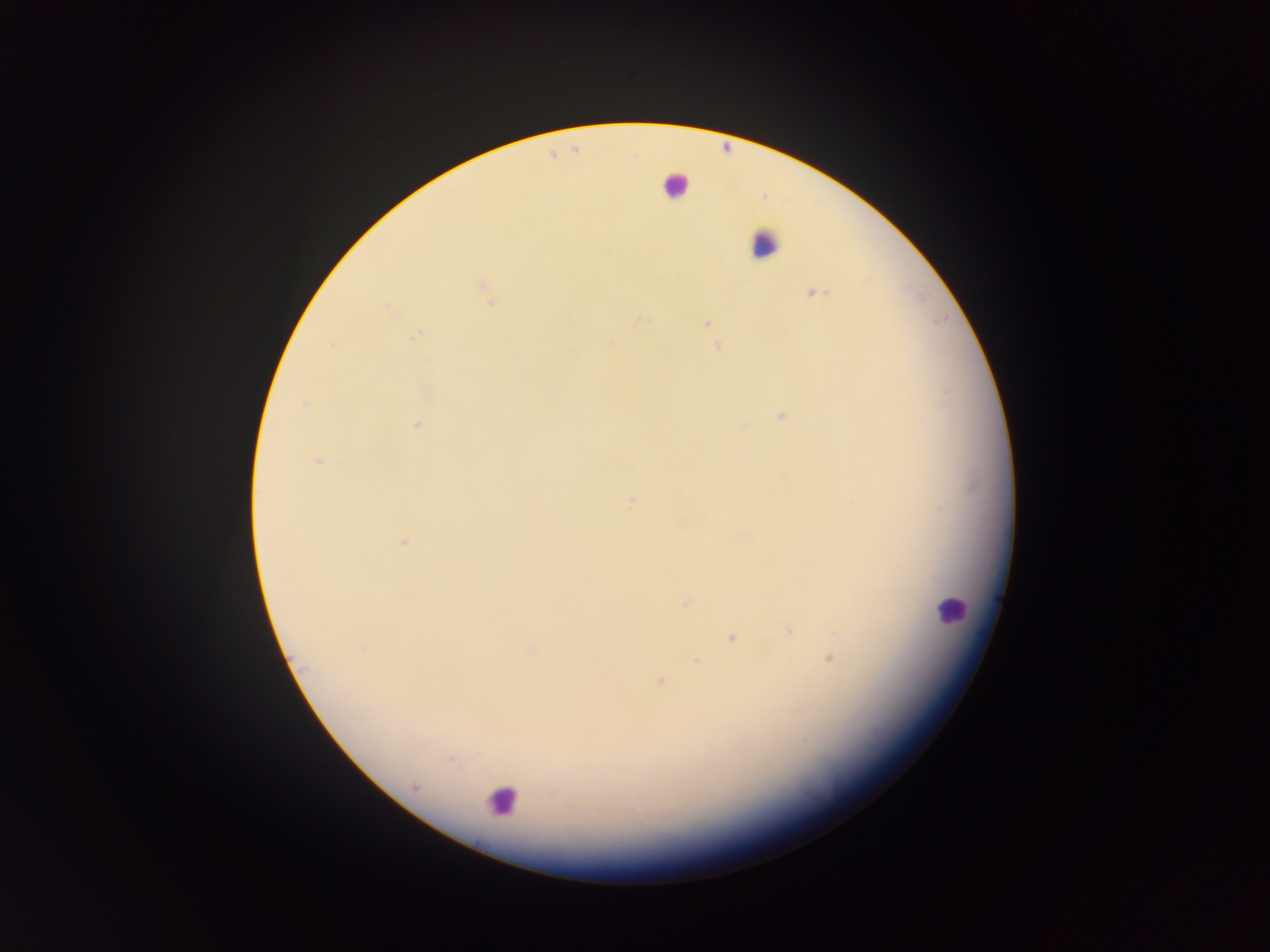 Approximate centers as [x, y] in pixels. Malaria parasite locations (subset; some below the resolvable size): [483, 287], [815, 293], [490, 302], [389, 309], [640, 320], [706, 324], [417, 335], [611, 343], [332, 345], [717, 347], [574, 350], [303, 404], [782, 416], [417, 426], [319, 462], [405, 542], [685, 604], [788, 631], [731, 638], [362, 650], [532, 650], [830, 659], [695, 660], [660, 682], [415, 787], [552, 794]. Leukocyte locations: [675, 185], [763, 245], [951, 608], [501, 800]. One field of view. Thick blood film. Image is 1270×952 pixels. Mobile-phone photograph taken through the microscope. Collected in Ghana.